Name the blood parasite species.
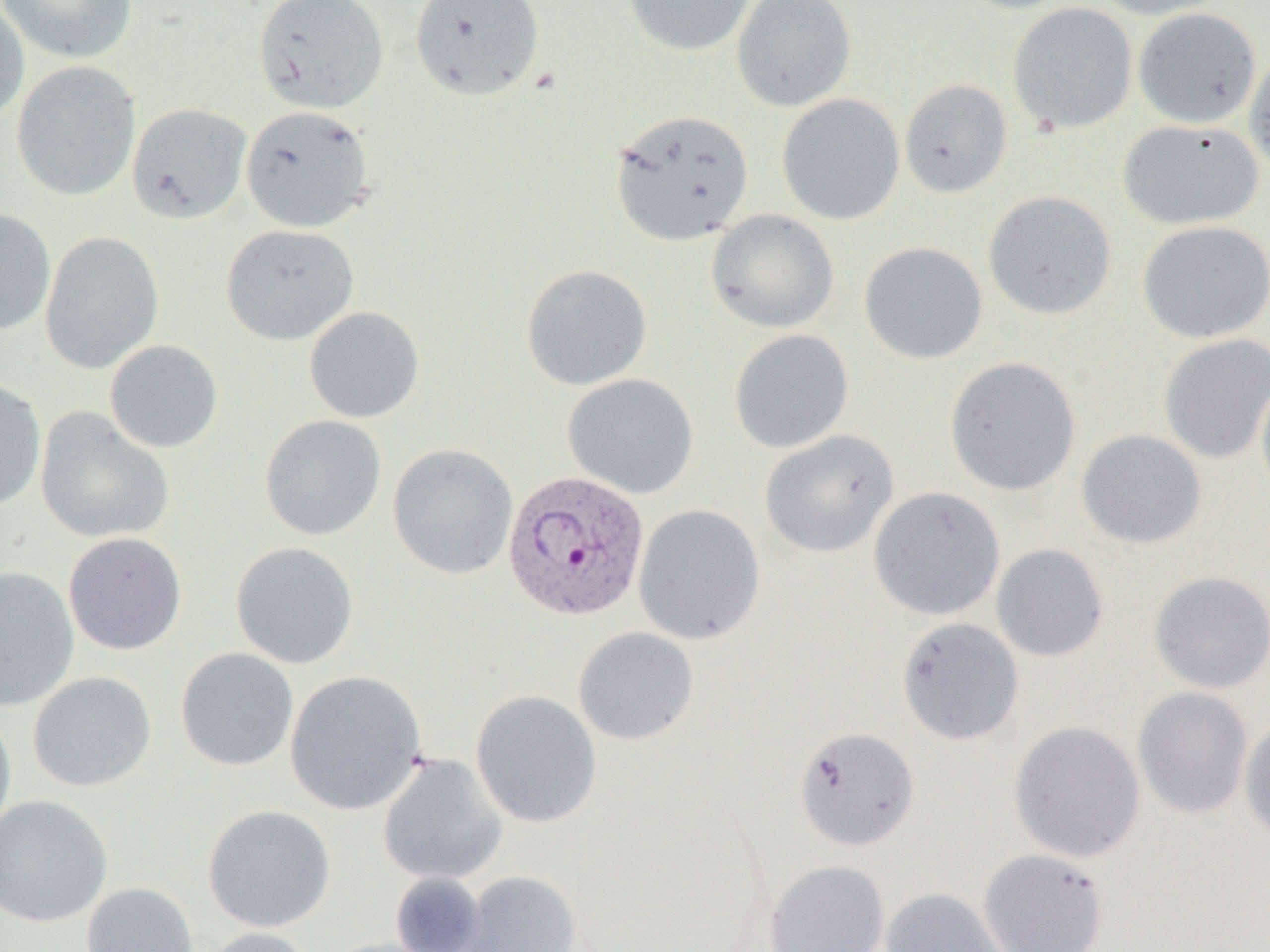
Plasmodium vivax.

uninfected red blood cell locations = approximate bounding boxes as (x1,y1)-(x2,y2) corner pairs in pixels: (0,0)-(138,64), (253,0)-(390,114), (408,0)-(546,102), (621,0)-(758,58), (731,0)-(857,113), (951,0)-(1084,14), (1088,0)-(1234,20), (0,1)-(29,124), (1007,2)-(1138,134), (1132,7)-(1262,129), (1243,47)-(1270,177), (11,61)-(141,202), (899,79)-(1013,198), (776,93)-(905,225), (127,103)-(253,224), (239,105)-(376,234), (609,108)-(755,247), (1117,118)-(1264,231), (983,190)-(1117,320), (0,207)-(57,335), (706,209)-(840,333), (1136,220)-(1270,343), (220,224)-(359,346), (40,231)-(164,375), (858,241)-(989,365), (521,264)-(653,391), (303,305)-(425,423), (729,329)-(854,454), (1158,333)-(1270,464), (104,339)-(224,454), (944,357)-(1081,495), (1255,371)-(1270,500), (562,373)-(699,499), (0,377)-(47,512), (34,407)-(174,544), (258,415)-(387,541), (759,429)-(899,558), (1076,429)-(1207,549), (387,443)-(518,580), (868,486)-(1006,621), (633,504)-(766,645), (63,531)-(187,655), (230,542)-(359,669), (991,543)-(1109,662), (0,566)-(80,712), (1149,570)-(1270,694), (896,617)-(1025,745), (573,627)-(699,745), (175,647)-(299,772), (284,670)-(427,814), (26,671)-(157,792), (1132,686)-(1254,820), (470,689)-(602,828), (0,705)-(17,844), (1239,715)-(1270,847), (1008,720)-(1146,862), (793,726)-(919,851), (377,753)-(507,885), (0,794)-(114,928), (202,804)-(336,933), (978,848)-(1110,952), (764,859)-(890,952), (458,870)-(583,952), (390,871)-(488,951), (81,881)-(198,952), (881,887)-(1009,952), (197,927)-(323,952)
Plasmodium vivax-infected red blood cell locations = approximate bounding boxes as (x1,y1)-(x2,y2) corner pairs in pixels: (502,469)-(650,621)
preparation = thin blood film
image size = 1270×952 pixels
magnification = 1000x
modality = optical microscopy
field of view = one of a larger specimen